State which parasite is depicted.
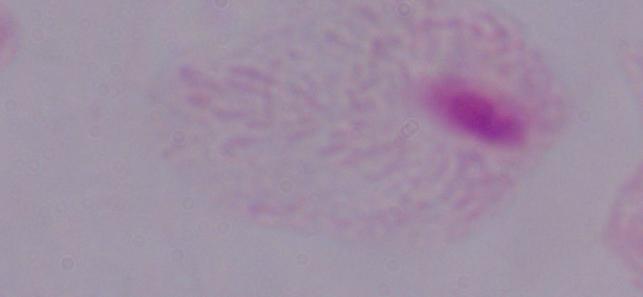

A trichomonad.

Micrograph. Captured at 1000x magnification.